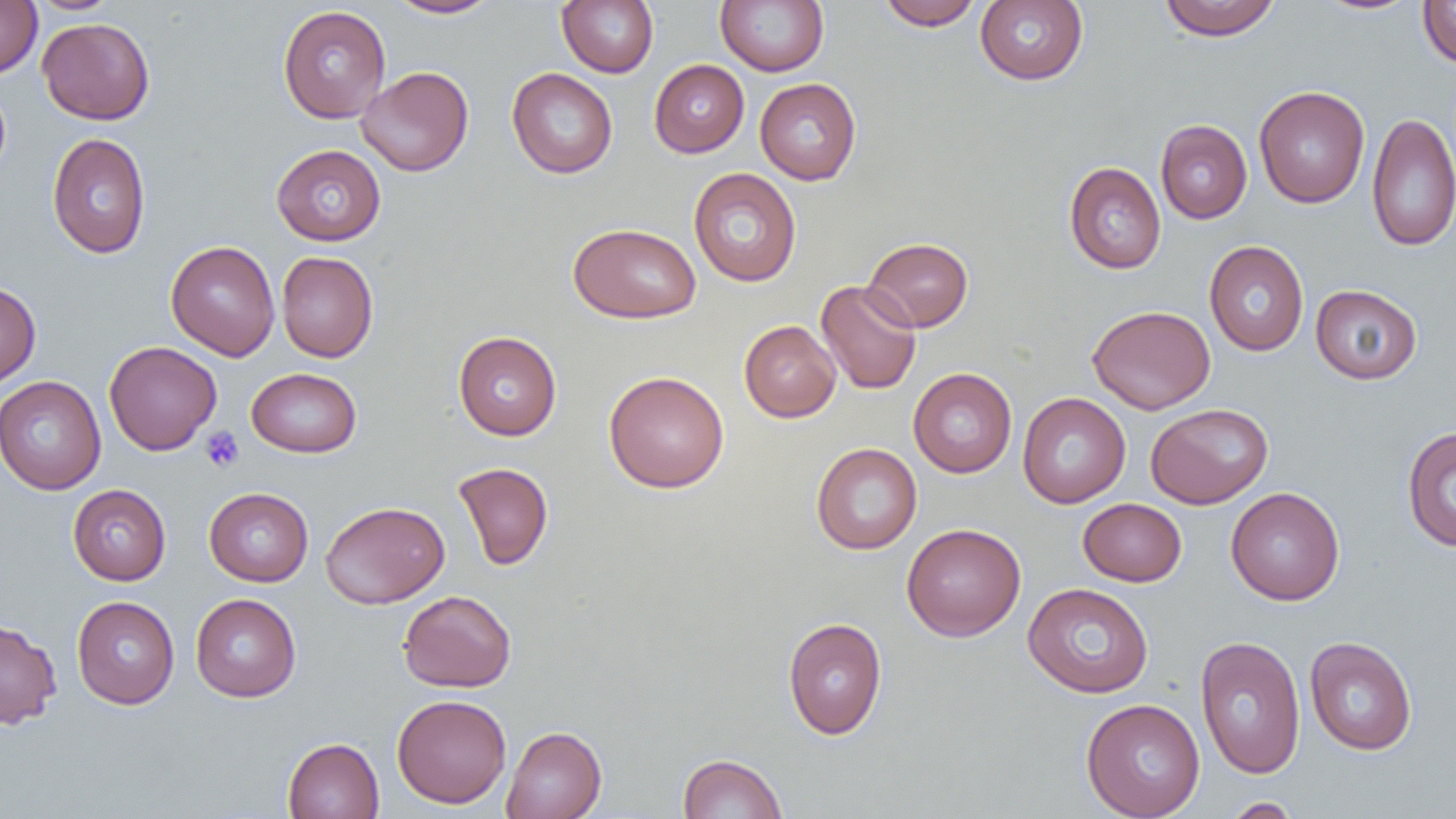
Approximate bounding boxes as (x1, y1, x2, y2) in pixels. Uninfected red blood cell locations: (0, 0, 42, 78), (386, 0, 501, 18), (556, 0, 658, 77), (715, 0, 828, 76), (876, 0, 983, 30), (1158, 0, 1282, 41), (1312, 0, 1423, 16), (26, 1, 122, 15), (974, 1, 1089, 86), (1417, 1, 1456, 68), (277, 5, 391, 123), (37, 18, 155, 124), (649, 59, 749, 157), (357, 66, 473, 177), (507, 67, 618, 179), (754, 77, 862, 185), (0, 80, 11, 185), (1254, 85, 1370, 208), (1367, 112, 1456, 252), (1155, 119, 1252, 223), (47, 132, 151, 259), (271, 144, 386, 246), (1064, 161, 1166, 274), (688, 167, 802, 287), (568, 222, 701, 324), (862, 237, 973, 332), (165, 240, 280, 360), (1204, 240, 1309, 356), (276, 251, 378, 362), (815, 279, 922, 395), (0, 280, 41, 388), (1310, 284, 1422, 385), (1087, 305, 1215, 414), (739, 320, 841, 422), (453, 331, 562, 440), (104, 341, 222, 455), (908, 367, 1017, 477), (246, 368, 362, 458), (603, 370, 729, 493), (0, 375, 106, 495), (1017, 392, 1130, 508), (1145, 403, 1273, 509), (1401, 425, 1456, 552), (811, 442, 922, 555), (453, 462, 554, 570), (67, 484, 171, 585), (204, 487, 313, 586), (1225, 487, 1345, 605), (1078, 498, 1187, 586), (320, 500, 449, 608), (901, 523, 1026, 641), (1023, 582, 1154, 698), (398, 590, 516, 692), (190, 593, 301, 702), (71, 595, 179, 709), (783, 617, 887, 739), (0, 618, 62, 729), (1195, 635, 1306, 779), (1304, 636, 1418, 755), (392, 694, 511, 808), (1081, 698, 1205, 819), (502, 725, 607, 819), (282, 737, 384, 819), (677, 753, 788, 818), (1223, 797, 1301, 818). Platelet locations: (201, 426, 244, 472). Slide-level diagnosis: negative for blood parasites. Light microscopy. Captured at 1000x magnification. Image is 1456×819 pixels. Thin blood film. One field of a larger specimen.